State which parasite is depicted.
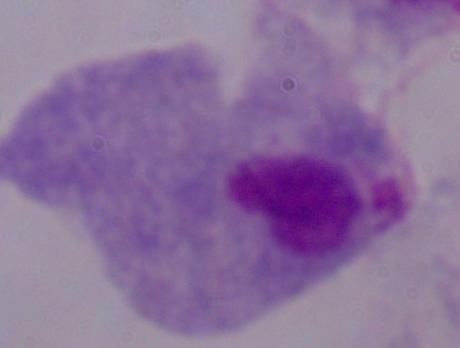

A trichomonad.

modality: micrograph
magnification: 1000x